Give the extent of all uninfected red blood cells.
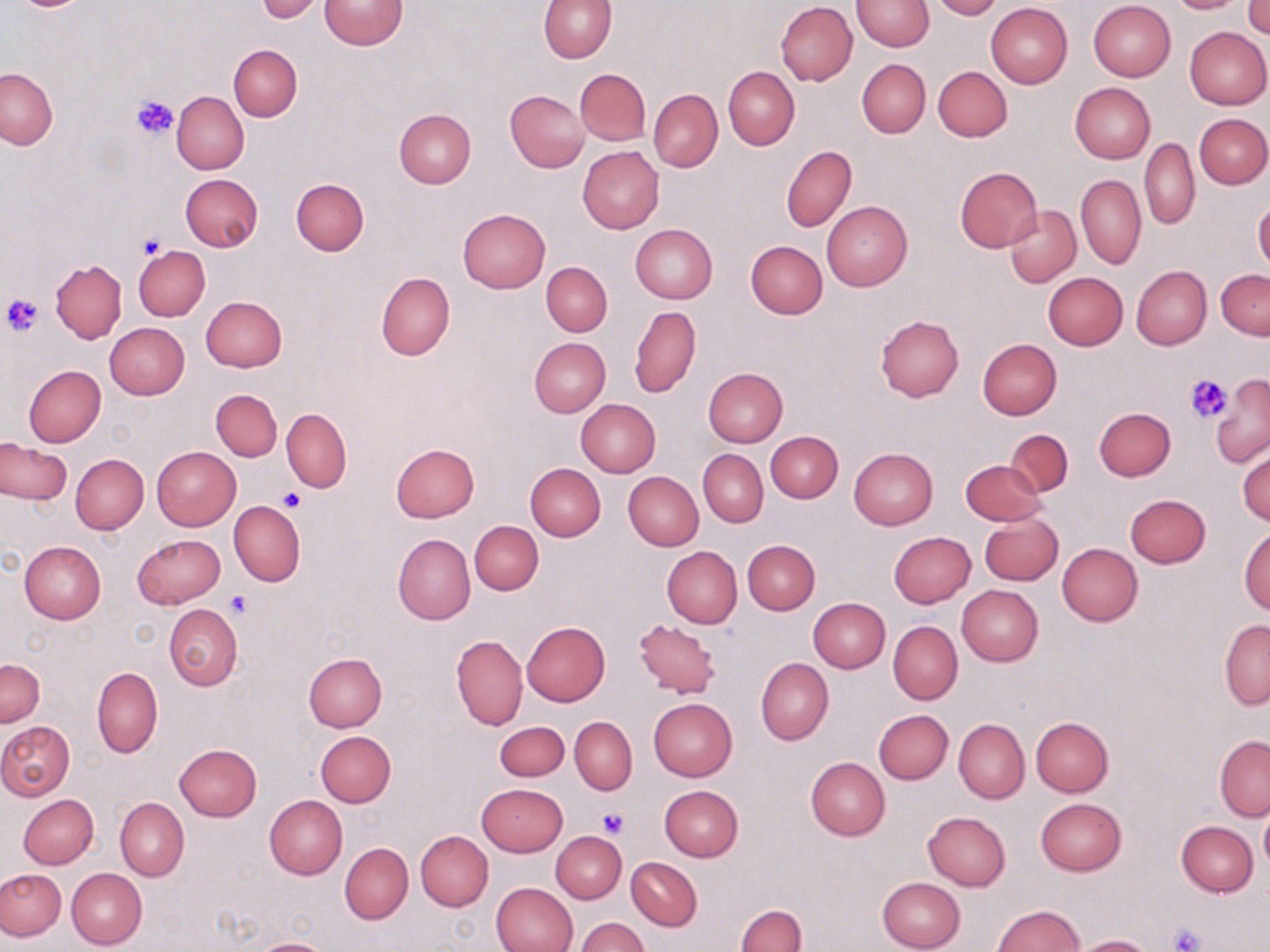
Approximate bounding boxes as [x1, y1, x2, y2] in pixels.
Uninfected red blood cells: [318, 0, 407, 51], [539, 0, 616, 63], [851, 0, 935, 50], [929, 0, 1002, 20], [1167, 0, 1246, 13], [256, 1, 326, 22], [1088, 1, 1175, 81], [775, 2, 857, 86], [1243, 2, 1270, 38], [986, 3, 1073, 88], [1184, 26, 1269, 109], [229, 45, 302, 121], [857, 59, 930, 138], [932, 66, 1012, 141], [1, 67, 57, 150], [723, 67, 799, 149], [575, 69, 651, 145], [1070, 82, 1156, 164], [648, 89, 723, 172], [172, 90, 249, 174], [505, 90, 589, 173], [393, 108, 475, 188], [1195, 113, 1270, 189], [1140, 137, 1200, 229], [781, 145, 856, 232], [578, 146, 664, 233], [955, 167, 1043, 252], [179, 174, 263, 252], [1076, 175, 1145, 270], [290, 178, 369, 256], [1254, 200, 1270, 276], [822, 201, 912, 290], [1004, 205, 1081, 287], [457, 208, 551, 293], [630, 223, 718, 304], [745, 241, 828, 319], [133, 245, 209, 319], [50, 259, 127, 343], [541, 261, 612, 336], [1131, 265, 1211, 350], [1216, 270, 1270, 339], [1042, 272, 1128, 350], [376, 274, 455, 358], [200, 295, 287, 371], [629, 305, 701, 398], [875, 315, 964, 401], [105, 322, 190, 400], [529, 338, 610, 417], [977, 338, 1061, 419], [24, 365, 106, 446], [703, 368, 788, 447], [1210, 374, 1270, 467], [211, 389, 282, 461], [576, 399, 660, 477], [1093, 407, 1175, 480], [281, 408, 351, 493], [1005, 429, 1073, 497], [766, 431, 843, 503], [1, 439, 72, 504], [390, 442, 479, 523], [1236, 443, 1269, 527], [152, 446, 240, 530], [849, 447, 938, 529], [697, 449, 768, 527], [70, 455, 148, 535], [960, 460, 1048, 526], [525, 463, 606, 541], [623, 472, 703, 551], [1124, 494, 1211, 568], [228, 500, 305, 587], [979, 513, 1062, 585], [470, 521, 543, 595], [1239, 526, 1270, 613], [889, 531, 975, 607], [133, 533, 226, 608], [392, 533, 475, 625], [742, 539, 820, 614], [19, 541, 106, 624], [1057, 542, 1143, 626], [662, 546, 742, 628], [956, 585, 1044, 666], [807, 598, 890, 673], [163, 603, 243, 690], [633, 619, 722, 699], [1219, 619, 1270, 709], [522, 621, 610, 706], [888, 621, 962, 704], [452, 635, 527, 730], [303, 653, 387, 732], [756, 657, 833, 745], [1, 659, 44, 727], [92, 667, 162, 757], [648, 697, 738, 781], [874, 709, 953, 784], [1030, 716, 1114, 796], [569, 717, 637, 795], [954, 718, 1029, 804], [0, 721, 75, 800], [495, 721, 570, 780], [315, 730, 396, 807], [1214, 736, 1270, 821], [174, 744, 262, 821], [804, 756, 890, 841], [476, 784, 567, 857], [659, 785, 743, 861], [19, 794, 99, 868], [264, 795, 347, 879], [116, 797, 189, 881], [1036, 798, 1126, 876], [1259, 806, 1270, 877], [922, 812, 1010, 891], [1176, 821, 1258, 897], [416, 830, 493, 911], [552, 831, 626, 903], [340, 844, 413, 923], [626, 857, 703, 931], [67, 867, 146, 949], [0, 868, 66, 941], [877, 877, 966, 952], [490, 882, 577, 952], [736, 904, 805, 952], [993, 905, 1085, 951], [576, 918, 649, 952], [1074, 935, 1154, 952], [250, 938, 337, 952].

Summary:
  - Platelet locations: [131, 94, 179, 141], [139, 233, 168, 259], [3, 293, 45, 335], [1185, 374, 1232, 423], [278, 489, 305, 512], [226, 589, 255, 619], [600, 808, 629, 836], [1169, 924, 1204, 952]
  - Slide-level diagnosis: no evidence of blood parasites
  - Stain: May-Grünwald-Giemsa
  - Image size: 1270×952 pixels
  - Preparation: thin blood smear
  - Field of view: one of a larger specimen
  - Magnification: 1000x
  - Modality: optical microscopy